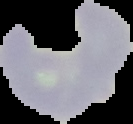
Segmented cell region on a black background. Image is 133×124 pixels. From a thin blood film. Result: no malaria parasites detected.